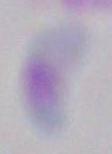
Captured at 1000x magnification. Toxoplasma gondii is shown. Micrograph.